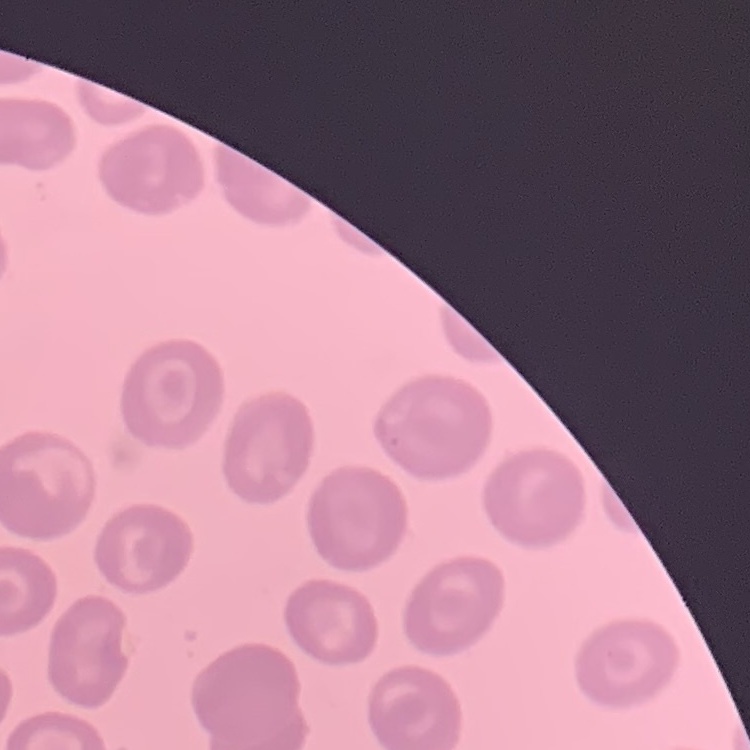
Summary:
  - Red blood cell morphology: no rouleaux formation
  - Image type: one tile cut from a larger photomicrograph
  - Preparation: thin blood smear
  - Stain: Field's or Giemsa